Identify the parasite.
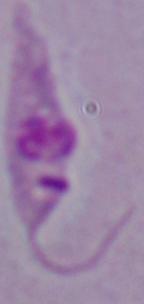
Leishmania.

modality: photomicrograph
magnification: 1000x